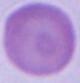

Summary:
  - Identification: red blood cell
  - Magnification: 1000x
  - Modality: photomicrograph